Assess the morphology of the red blood cells.
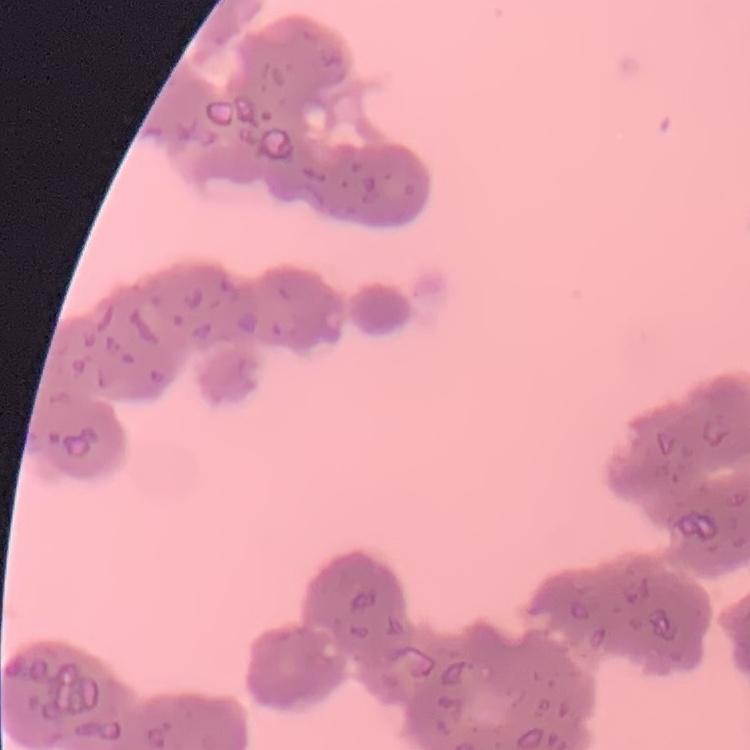
They show rouleaux formation.

{
  "stain": "Field's or Giemsa",
  "preparation": "thin peripheral smear",
  "image_type": "one tile cut from a larger photomicrograph"
}